Assess the morphology of the red blood cells.
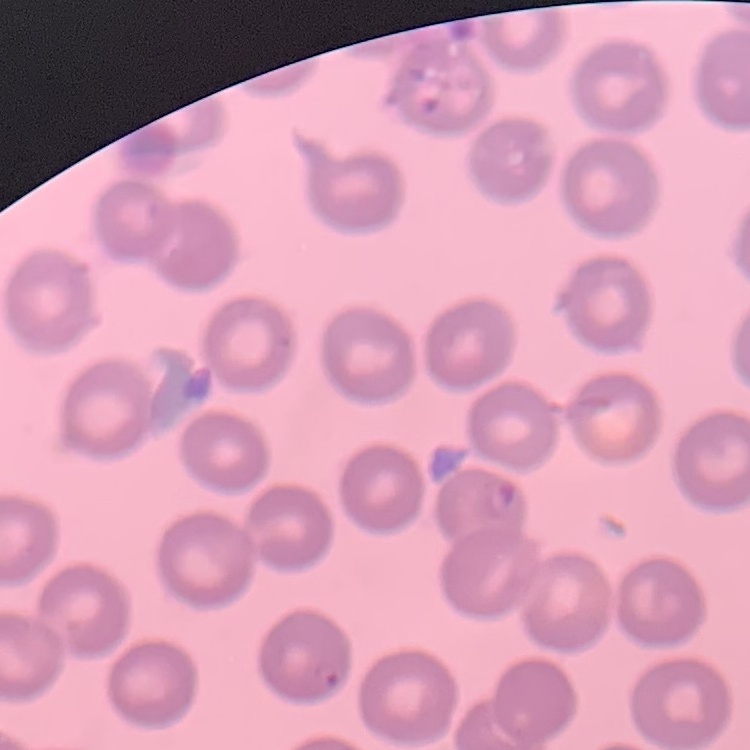

They show no rouleaux formation.

Square crop of a larger photomicrograph. Field's or Giemsa stain. Thin peripheral smear.